Identify the blood parasite species.
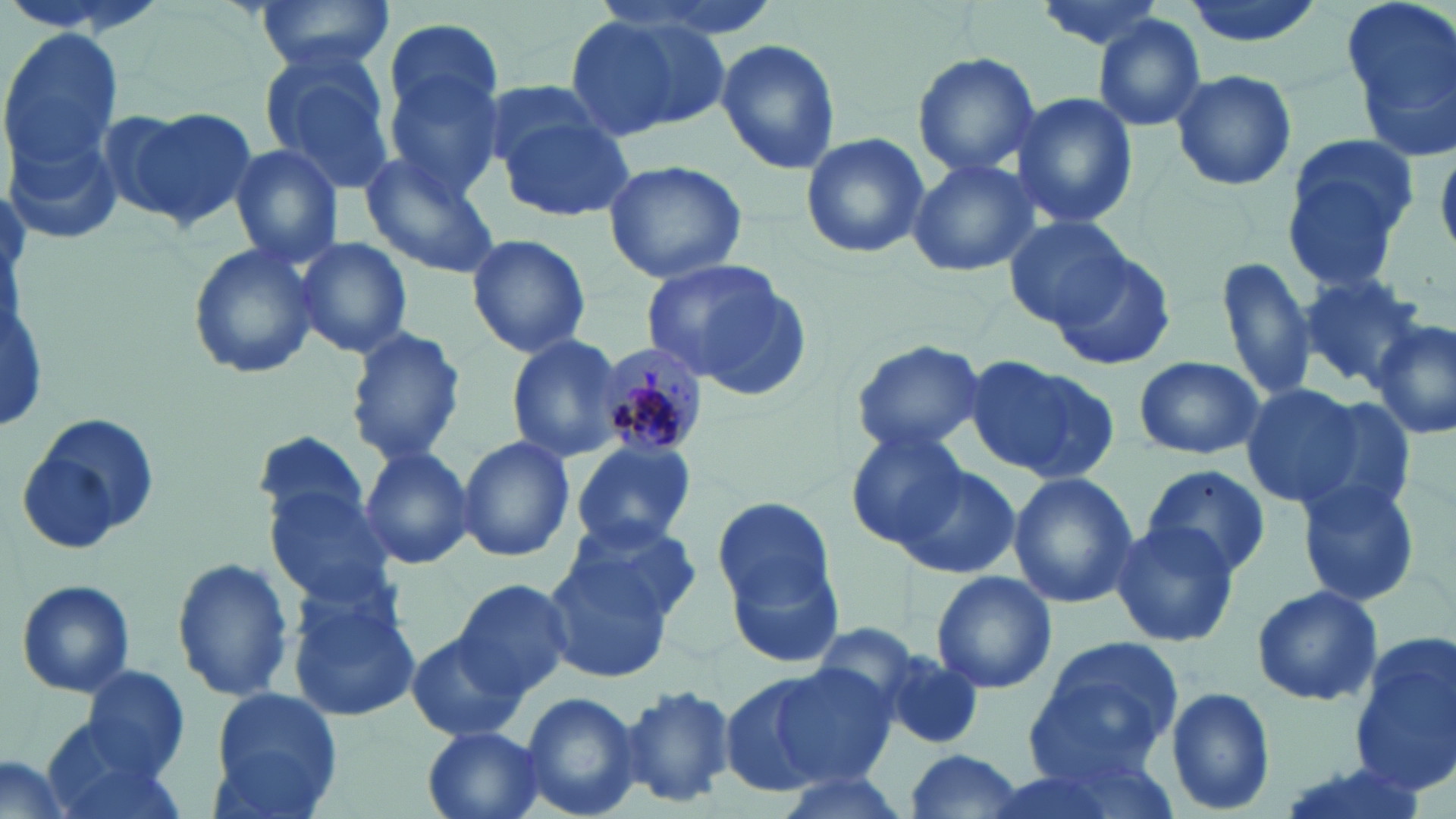

Plasmodium malariae.

Approximate bounding boxes as (x1,y1)-(x2,y2) corner pairs in pixels. Plasmodium malariae-infected red blood cell locations: (594,340)-(712,462). Uninfected red blood cell locations: (2,0)-(167,40), (248,0)-(398,74), (1035,0)-(1170,54), (1178,0)-(1326,47), (1343,0)-(1456,152), (561,10)-(737,140), (1092,13)-(1207,132), (382,18)-(503,135), (0,29)-(128,178), (715,38)-(840,176), (258,47)-(398,195), (911,51)-(1041,177), (385,68)-(504,197), (1170,68)-(1296,192), (478,78)-(618,181), (1013,92)-(1138,230), (113,104)-(260,234), (497,104)-(635,223), (9,131)-(123,248), (800,132)-(930,258), (1281,133)-(1423,282), (227,143)-(342,270), (361,151)-(501,277), (906,157)-(1037,276), (602,159)-(748,284), (1006,217)-(1132,325), (465,232)-(592,357), (293,237)-(411,359), (187,240)-(321,380), (1050,249)-(1178,373), (1217,255)-(1316,404), (640,258)-(805,392), (1299,273)-(1427,385), (1369,321)-(1455,443), (346,326)-(467,466), (505,335)-(628,464), (850,339)-(986,456), (1131,357)-(1267,459), (966,358)-(1118,482), (1240,384)-(1362,506), (1291,397)-(1421,522), (18,411)-(159,553), (844,430)-(970,548), (255,431)-(375,531), (457,436)-(576,563), (569,441)-(696,553), (359,446)-(475,572), (895,464)-(1022,581), (1141,464)-(1272,578), (1007,471)-(1138,611), (1292,477)-(1424,609), (262,481)-(398,609), (713,495)-(840,628), (558,519)-(699,625), (1110,520)-(1239,649), (547,552)-(678,680), (169,554)-(295,703), (930,569)-(1057,695), (453,577)-(575,696), (14,578)-(137,699), (1249,583)-(1384,708), (286,585)-(422,724), (803,622)-(923,726), (405,632)-(525,743), (1350,634)-(1456,796), (1024,639)-(1181,781), (881,653)-(988,752), (772,664)-(897,784), (78,665)-(190,776), (719,674)-(843,799), (616,683)-(737,809), (1164,685)-(1277,815), (208,687)-(343,816), (518,689)-(641,819), (421,727)-(548,819), (42,736)-(188,819), (899,751)-(1030,819), (1,757)-(71,819), (771,771)-(913,819). May-Grünwald-Giemsa stain. Image is 1456×819 pixels. 1000x magnification. Thin blood smear. Optical microscopy. One field of a larger specimen.